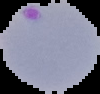
Summary:
  - Image size: 100×94 pixels
  - Preparation: thin blood film
  - Malaria status: parasitized
  - Image type: segmented cell region with the area outside set to black